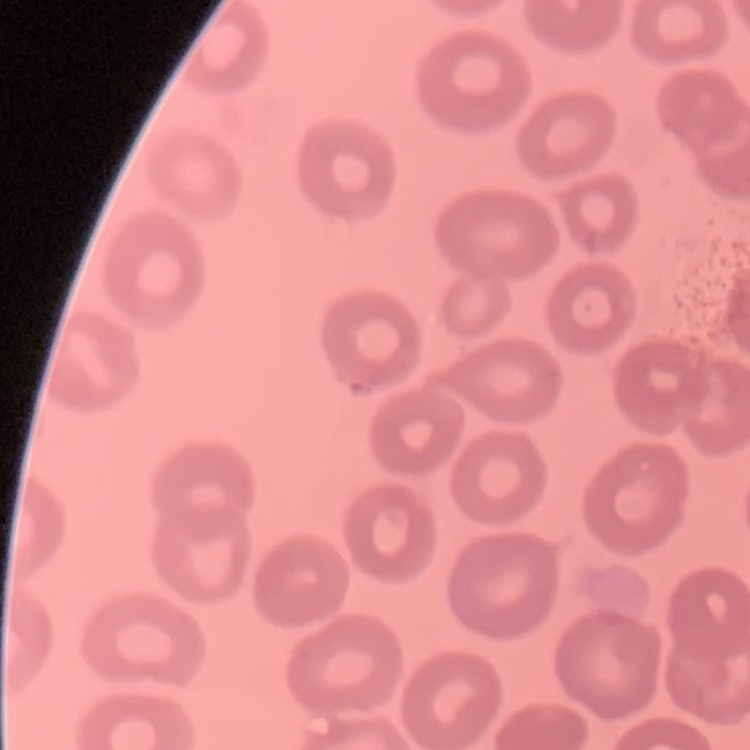
The erythrocytes exhibit no rouleaux formation. Thin peripheral smear. Stained with either Field's or Giemsa. One tile cut from a larger photomicrograph.